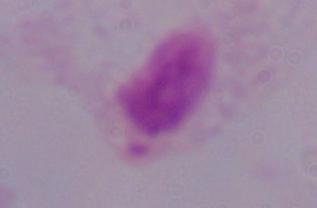

Summary:
  - Magnification: 1000x
  - Identification: trichomonad
  - Modality: micrograph